Classify this cell by malaria status.
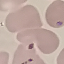

Uninfected.

capture = smartphone through the microscope eyepiece
image type = automatically extracted cell patch, resized to 64 × 64 pixels
stain = Giemsa
preparation = thin blood smear